Report the malaria status of this cell.
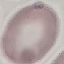
Uninfected.

image type = automatically extracted cell patch, resized to 64 × 64 pixels
stain = Giemsa
capture = smartphone camera at the microscope eyepiece
preparation = thin blood film